Classify this cell by malaria status.
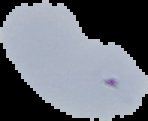

It is uninfected.

Summary:
  - Preparation: thin blood smear
  - Image type: segmented cell region with the area outside set to black
  - Image size: 148×121 pixels